Identify the cell.
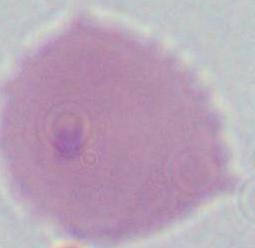
This is an erythrocyte.

Captured at 1000x magnification. Photomicrograph.